Outline each Plasmodium vivax-infected red blood cell.
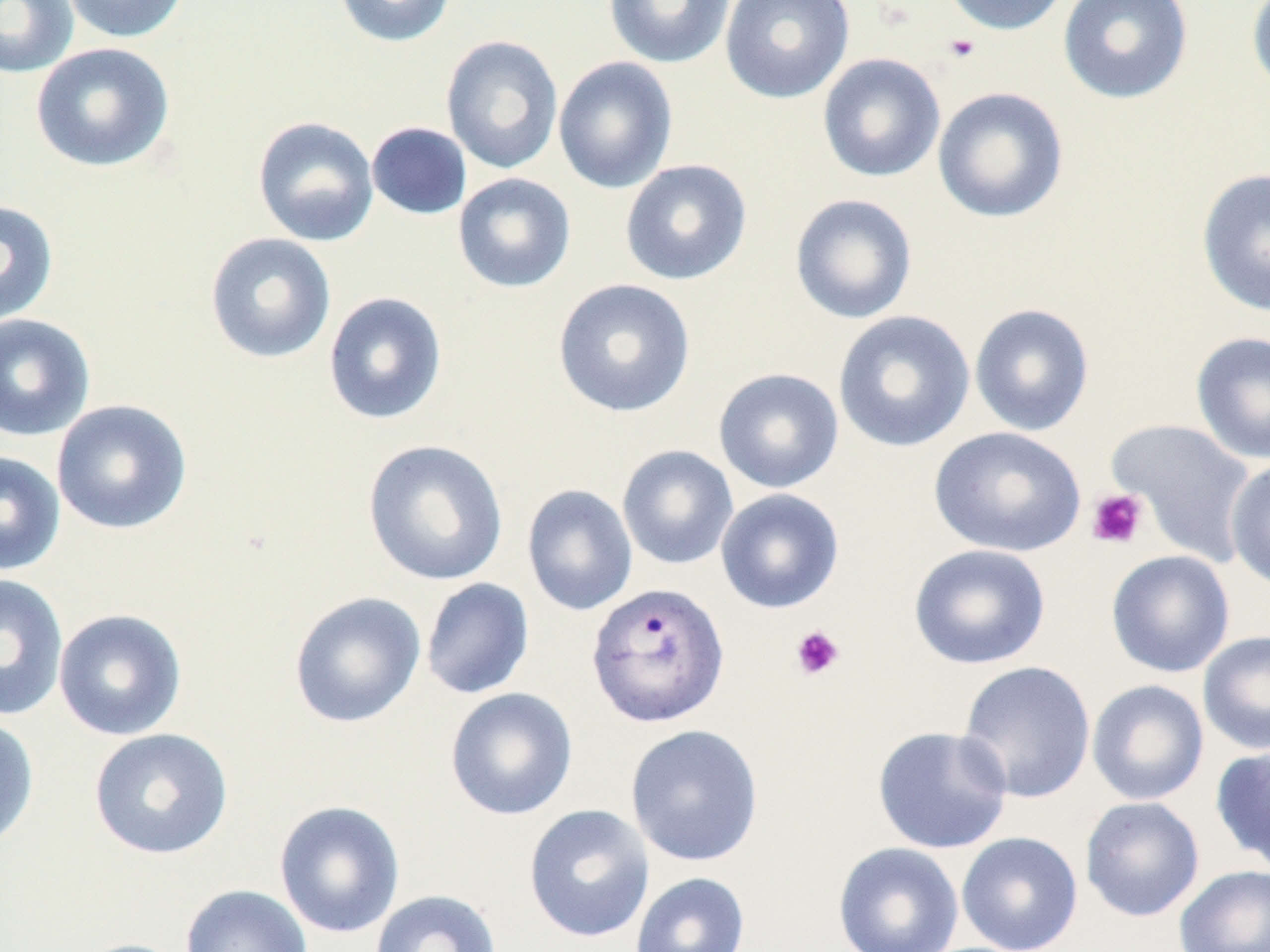
Approximate bounding boxes as (x1,y1)-(x2,y2) corner pairs in pixels.
Plasmodium vivax-infected red blood cells: (586,582)-(730,728).

Summary:
  - Platelet locations (subset): (942,33)-(981,63), (1086,488)-(1149,550), (790,624)-(845,680)
  - Uninfected red blood cell locations (subset): (0,0)-(79,79), (59,0)-(191,44), (331,0)-(458,48), (603,0)-(736,69), (719,0)-(855,104), (940,0)-(1073,36), (1057,0)-(1194,105), (1246,1)-(1270,96), (440,35)-(564,175), (30,41)-(175,173), (817,53)-(946,183), (553,56)-(678,194), (932,86)-(1069,224), (251,115)-(380,247), (365,121)-(473,221), (619,159)-(753,286), (1196,167)-(1270,318), (452,173)-(576,294), (789,193)-(918,324), (0,199)-(59,327), (204,232)-(337,365), (552,278)-(696,418), (323,291)-(448,426), (969,303)-(1095,437), (832,310)-(976,453), (0,313)-(96,441), (1190,330)-(1270,466), (713,368)-(844,494), (51,398)-(193,535), (928,426)-(1086,557), (362,438)-(509,586), (616,445)-(739,570), (0,451)-(66,575), (1225,457)-(1270,593), (522,484)-(638,616), (715,488)-(845,614), (908,543)-(1051,670), (1105,550)-(1235,679), (0,573)-(69,722), (420,578)-(534,699), (288,591)-(426,729), (53,609)-(188,740), (1197,629)-(1270,756), (957,660)-(1096,804), (1086,679)-(1210,806), (445,687)-(578,821), (0,714)-(39,851), (625,724)-(764,867), (872,725)-(1013,854), (89,727)-(233,860), (1210,744)-(1270,871), (1080,796)-(1205,922), (273,800)-(405,939), (523,804)-(655,943), (956,831)-(1083,952), (832,842)-(964,952), (1174,865)-(1270,952), (629,871)-(751,952), (180,884)-(313,952), (370,889)-(503,952), (71,938)-(194,952)
  - Slide-level diagnosis: Plasmodium vivax
  - Modality: optical microscopy
  - Stain: May-Grünwald-Giemsa
  - Field of view: one of a larger specimen
  - Image size: 1270×952 pixels
  - Preparation: thin blood smear
  - Magnification: 1000x